Report the malaria status of this cell.
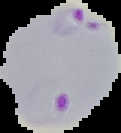
It is parasitized.

Summary:
  - Image type: cell region segmented out of the field of view; surrounding area masked to black
  - Preparation: thin blood smear
  - Image size: 121×133 pixels